Report the malaria status of this cell.
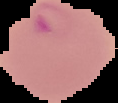

Parasitized.

Summary:
  - Preparation: thin blood film
  - Image size: 118×103 pixels
  - Image type: cell region segmented out of the field of view; surrounding area masked to black